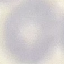

Result: no malaria parasites seen. Giemsa-stained preparation. Thin blood smear. Acquired by smartphone through the microscope eyepiece. Automatically extracted cell patch, resized to 64 × 64 pixels.